Give the position of every malaria parasite.
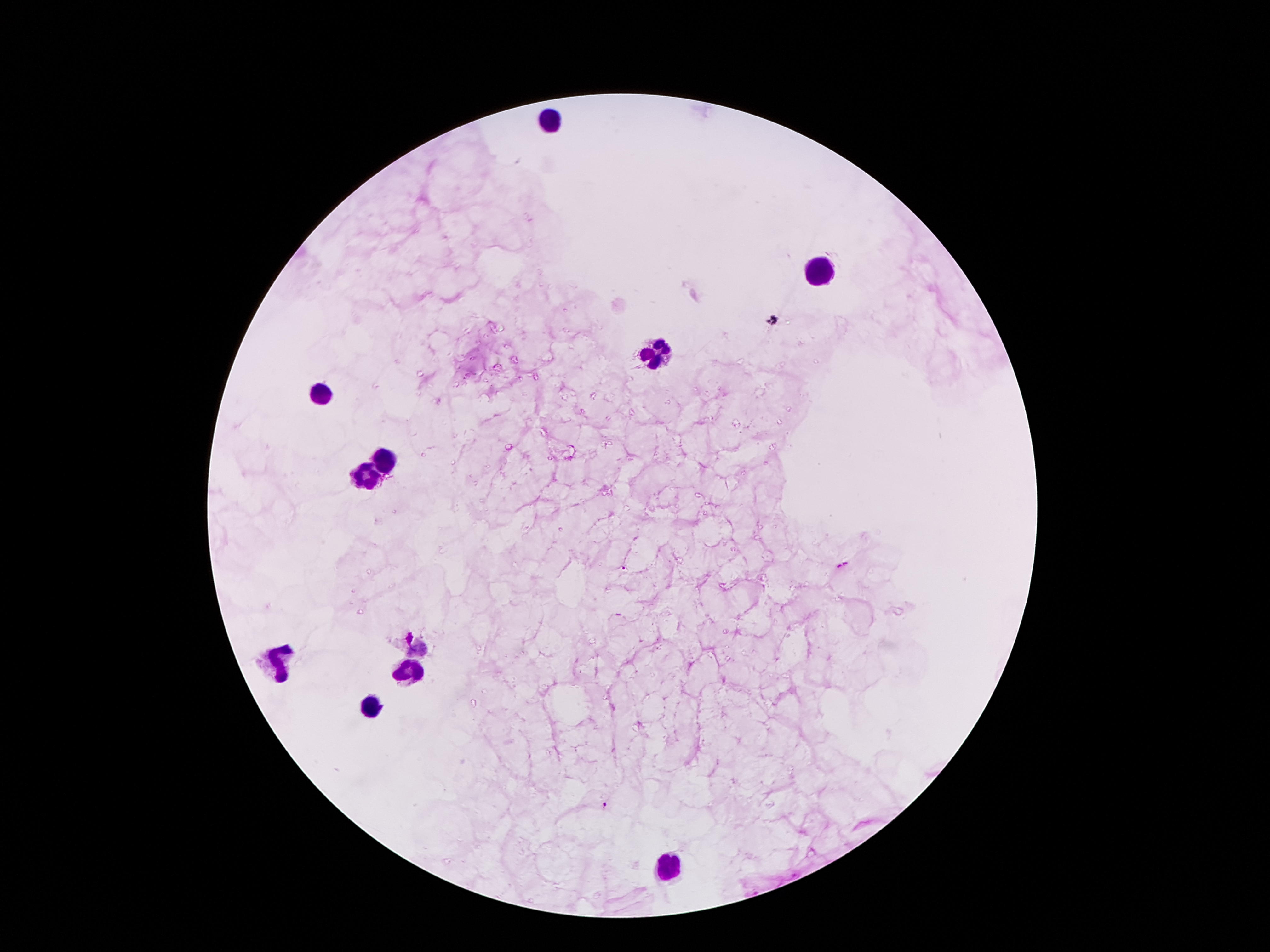
Approximate object centers, in pixels from the top-left corner.
Malaria parasites: (x=624, y=569), (x=605, y=805).

Leukocyte locations: (x=548, y=121), (x=821, y=272), (x=657, y=356), (x=321, y=396), (x=384, y=461), (x=365, y=476), (x=277, y=660), (x=410, y=671), (x=376, y=705), (x=668, y=870). Giemsa stain. Thick blood film. Photographed through the microscope eyepiece with a smartphone camera. Single field of view. Patient malaria status: infected with Plasmodium falciparum. 100x magnification. Image is 1270×952 pixels.